State which parasite is depicted.
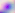
Toxoplasma gondii.

{
  "magnification": "400x",
  "modality": "photomicrograph"
}